State which parasite is depicted.
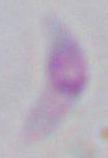

This is Toxoplasma gondii.

modality = micrograph
magnification = 1000x